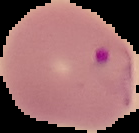
Summary:
  - Result: Plasmodium parasites detected
  - Image size: 139×133 pixels
  - Preparation: thin blood smear
  - Image type: cell region segmented out of the field of view; surrounding area masked to black